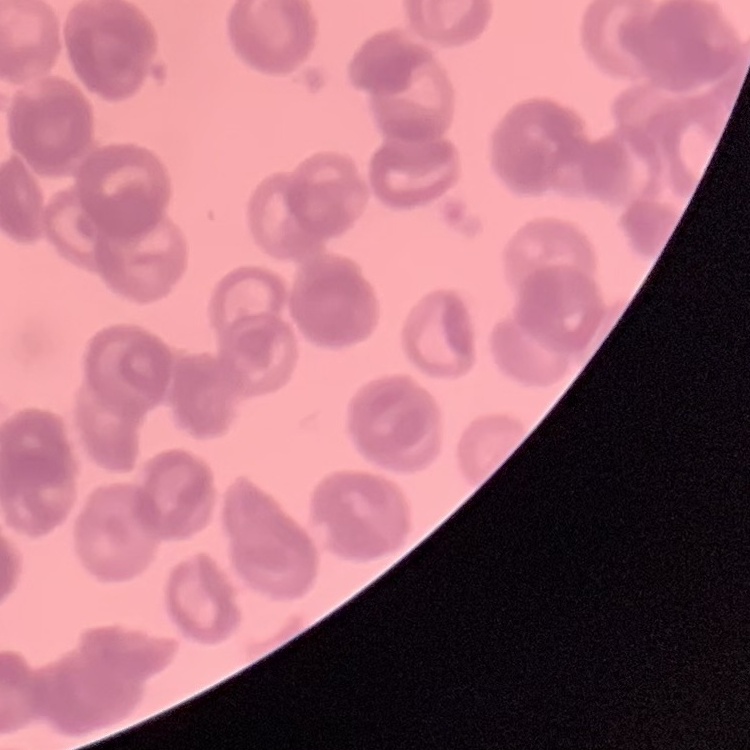
Summary:
  - Erythrocyte morphology: rouleaux formation
  - Image type: square crop of a larger photomicrograph
  - Preparation: thin blood smear
  - Stain: Field's or Giemsa